Classify this cell by malaria status.
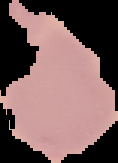

It is uninfected.

Segmented cell region on a black background. From a thin blood smear. Image is 118×163 pixels.